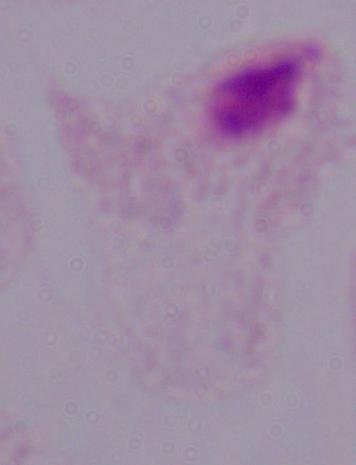

Photomicrograph. 1000x magnification. A trichomonad is shown.